Comment on the morphology of the erythrocytes.
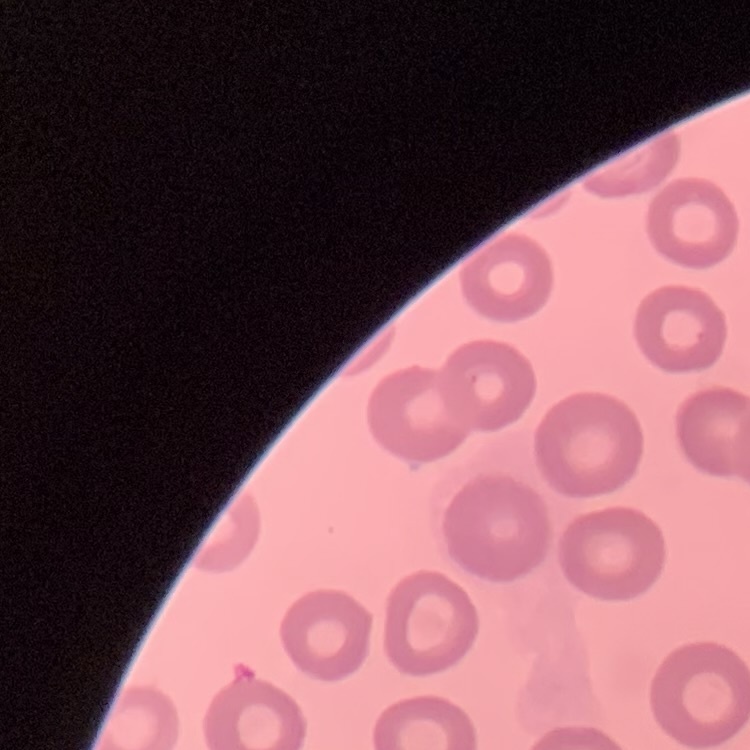

They show no rouleaux formation.

{
  "image_type": "one tile cut from a larger photomicrograph",
  "preparation": "thin peripheral smear",
  "stain": "Field's or Giemsa"
}